Name the parasite shown.
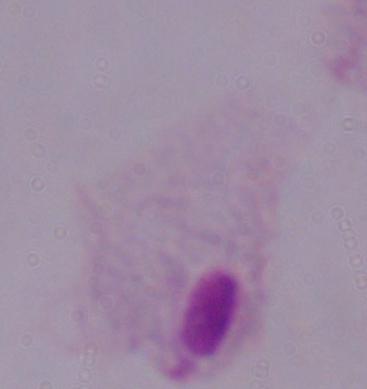
This is a trichomonad.

Summary:
  - Modality: photomicrograph
  - Magnification: 1000x